Report the malaria status of this cell.
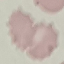
Uninfected.

stain = Giemsa
image type = automatically extracted cell patch, resized to 64 × 64 pixels
capture = smartphone camera at the microscope eyepiece
preparation = thin smear